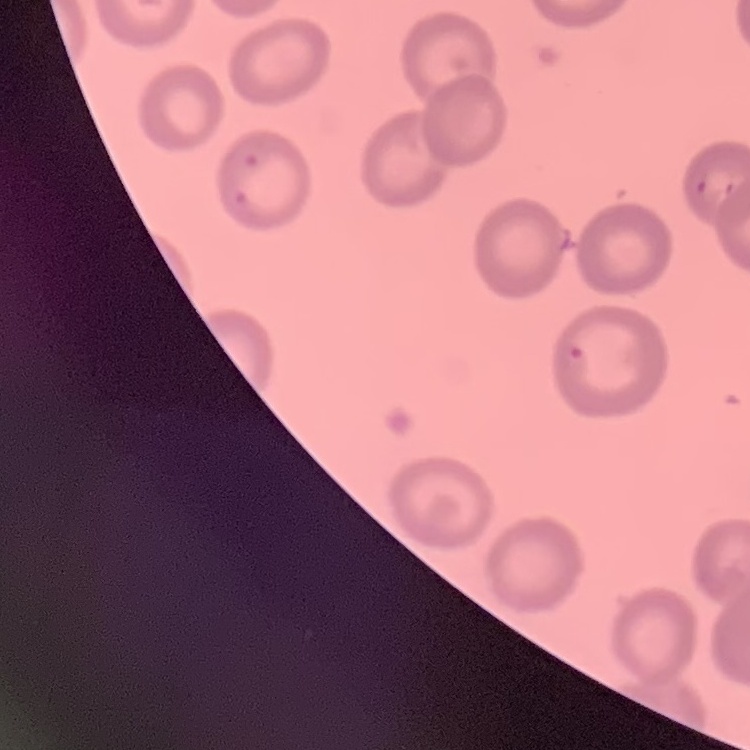
red_blood_cell_morphology: no rouleaux formation
image_type: square crop of a larger photomicrograph
preparation: thin blood film
stain: Field's or Giemsa